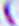
Summary:
  - Identification: Toxoplasma gondii
  - Magnification: 400x
  - Modality: photomicrograph